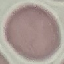

Malaria status: uninfected. Thin blood smear. Automatically extracted cell patch, resized to 64 × 64 pixels. Photographed with a smartphone camera at the microscope eyepiece. Giemsa-stained preparation.